Identify the parasite.
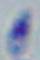

This is Toxoplasma gondii.

Micrograph. Captured at 1000x magnification.